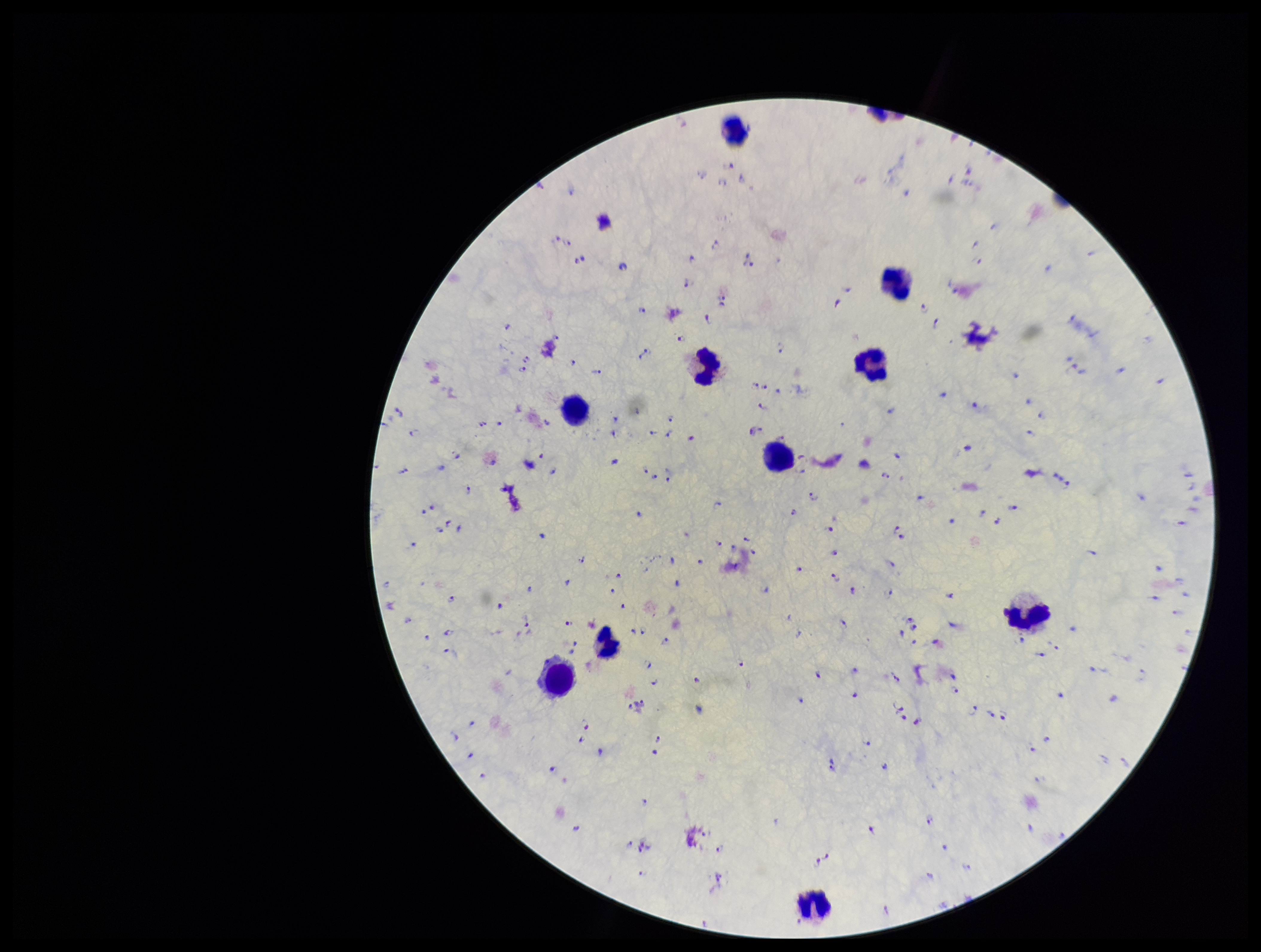
preparation = thick smear
capture = smartphone photograph through the microscope eyepiece
parasite count = 205
Plasmodium parasites = detected
species reported for this patient = Plasmodium falciparum
leukocyte count = 10
image size = 1261×952 pixels
patient malaria status = positive
field of view = one from this slide
stain = Giemsa